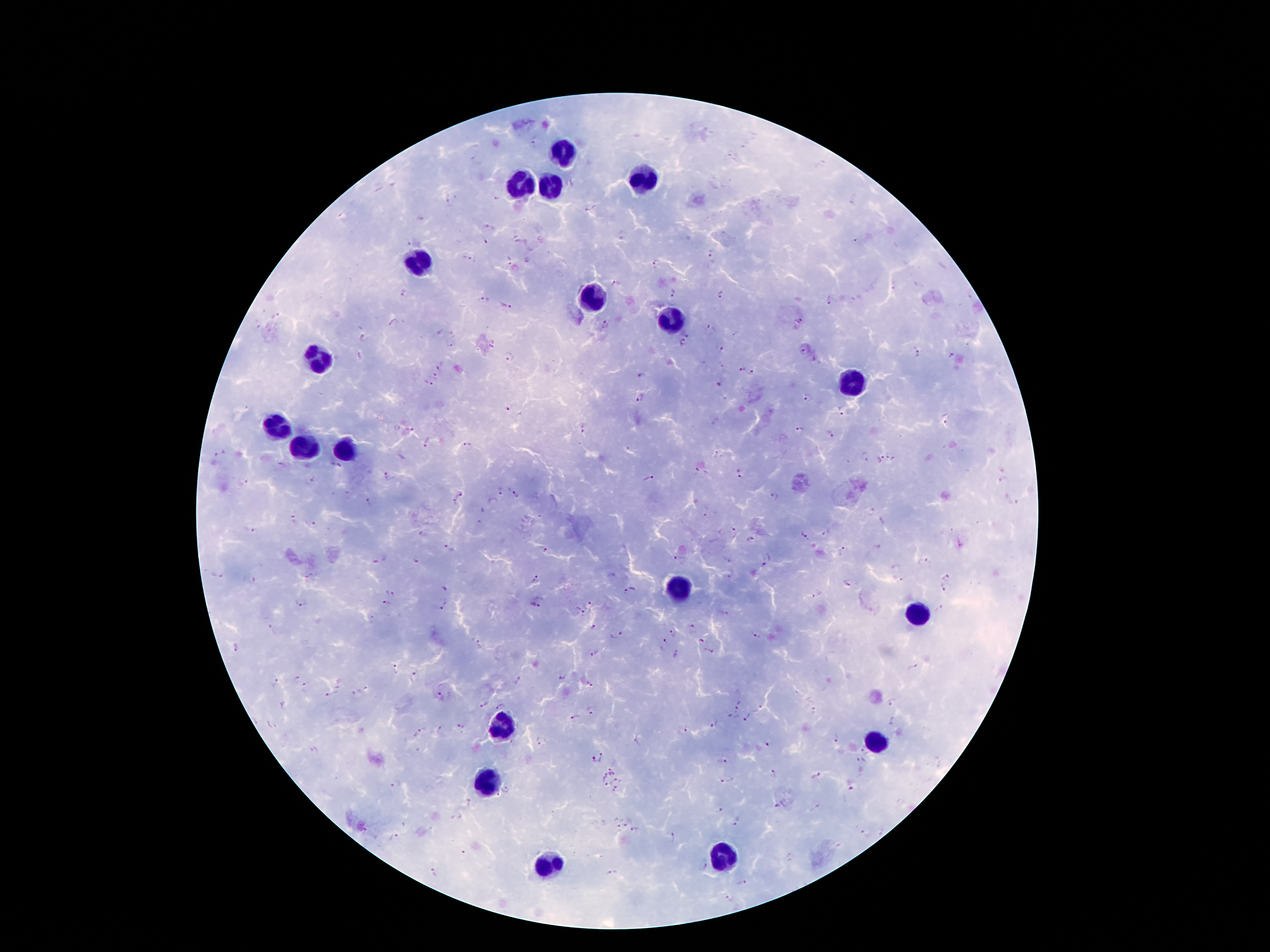
coordinate format = approximate centers as (x, y) in pixels
malaria parasite locations = (535, 144), (449, 203), (588, 208), (490, 227), (711, 253), (472, 259), (510, 261), (656, 264), (617, 284), (674, 292), (403, 293), (721, 295), (482, 299), (830, 299), (506, 306), (605, 324), (710, 330), (364, 338), (683, 343), (450, 344), (718, 349), (803, 351), (916, 354), (951, 354), (509, 358), (741, 369), (753, 372), (433, 376), (640, 376), (428, 383), (719, 385), (639, 398), (808, 398), (509, 407), (842, 411), (946, 419), (585, 428), (800, 429), (829, 432), (426, 443), (467, 445), (716, 454), (888, 454), (865, 456), (880, 458), (895, 460), (281, 465), (337, 466), (696, 471), (387, 476), (648, 478), (741, 478), (313, 480), (243, 482), (501, 491), (517, 495), (774, 496), (460, 498), (492, 501), (371, 502), (1013, 504), (705, 511), (294, 518), (316, 525), (250, 531), (734, 533), (827, 533), (424, 535), (804, 536), (751, 539), (878, 546), (449, 551), (843, 551), (544, 552), (769, 555), (727, 558), (680, 559), (415, 560), (924, 562), (762, 566), (731, 575), (218, 576), (946, 576), (254, 580), (535, 580), (849, 582), (943, 587), (444, 589), (625, 592), (390, 593), (816, 593), (590, 603), (302, 604), (389, 605), (535, 605), (445, 606), (579, 611), (692, 626), (594, 627), (271, 629), (617, 633), (673, 634), (756, 635), (701, 639), (665, 641), (480, 643), (235, 648), (708, 650), (595, 652), (677, 652), (913, 667), (394, 671), (562, 676), (414, 677), (297, 679), (517, 680), (276, 682), (590, 683), (305, 687), (331, 694), (440, 694), (502, 702), (892, 702), (486, 703), (741, 707), (592, 708), (575, 717), (733, 717), (748, 717), (894, 719), (714, 724), (462, 727), (440, 728), (683, 731), (420, 732), (837, 739), (540, 741), (770, 745), (315, 749), (864, 751), (603, 758), (591, 761), (723, 761), (861, 762), (613, 770), (772, 772), (816, 776), (602, 777), (726, 779), (616, 780), (395, 785), (606, 785), (851, 789), (614, 790), (508, 791), (470, 804), (779, 805), (720, 809), (628, 821), (736, 822), (617, 827), (636, 831), (881, 831), (864, 832), (397, 836), (671, 838), (703, 867), (433, 871), (612, 873), (743, 883), (730, 898)
leukocyte locations = (564, 149), (644, 178), (518, 183), (551, 185), (417, 262), (593, 298), (671, 319), (320, 355), (847, 384), (278, 429), (304, 447), (346, 449), (675, 592), (919, 611), (501, 727), (877, 741), (490, 786), (724, 851), (554, 865)
magnification = 100x
capture = smartphone camera through the microscope eyepiece
preparation = thick blood film
stain = Giemsa
image size = 1270×952 pixels
patient malaria status = positive for Plasmodium falciparum
field of view = single